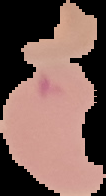

Summary:
  - Image size: 106×196 pixels
  - Preparation: thin blood smear
  - Image type: segmented cell region with the area outside set to black
  - Result: no malaria parasites seen